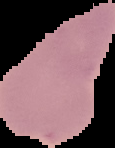
malaria_status: uninfected
image_size: 115×148 pixels
preparation: thin blood film
image_type: segmented cell region on a black background